Name the blood parasite species.
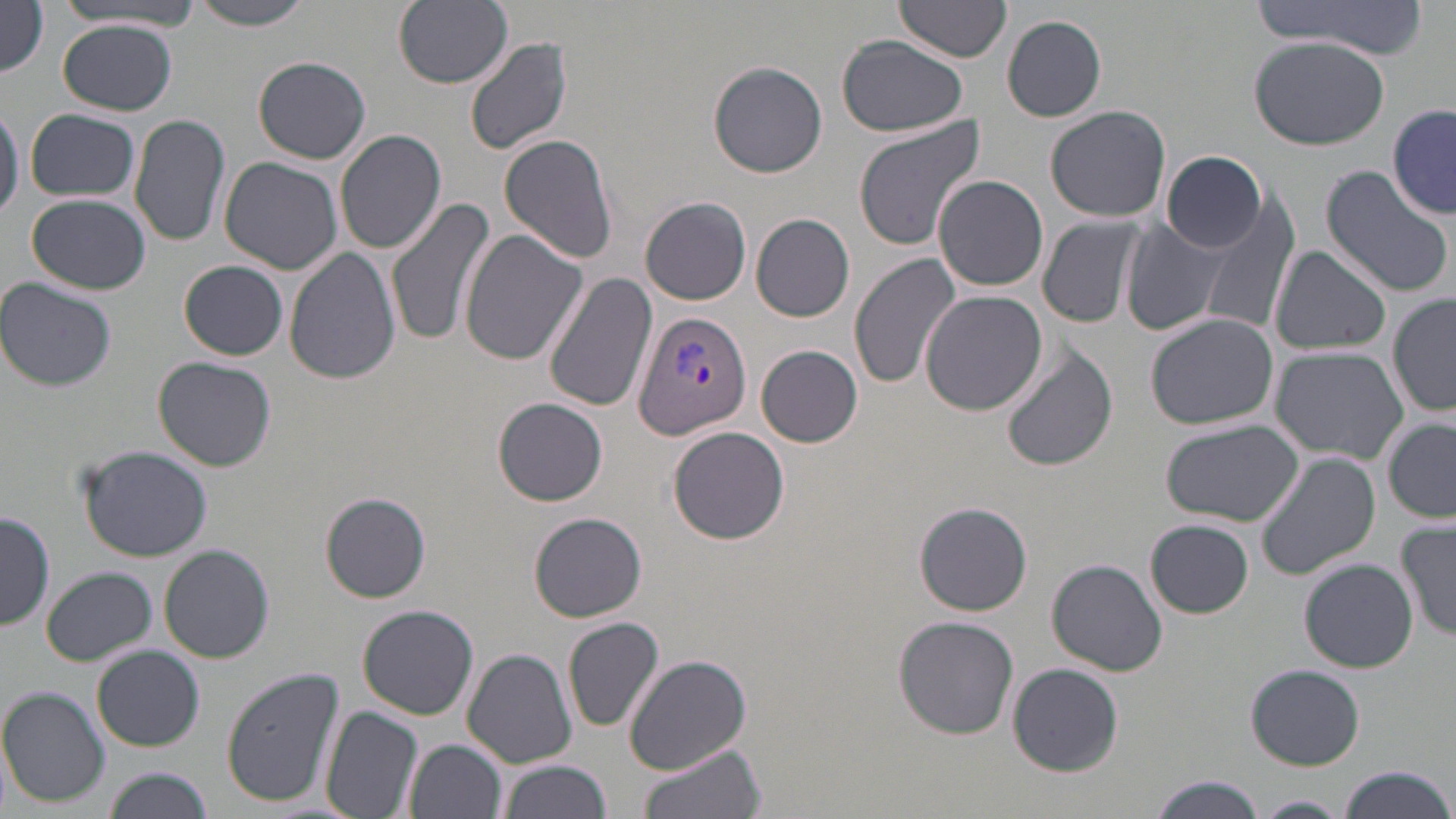

Plasmodium vivax.

Approximate bounding boxes as named x1/y1/x2/y2 corners in pixels. Plasmodium vivax-infected red blood cell locations: (x1=634, y1=312, x2=752, y2=437). Uninfected red blood cell locations: (x1=395, y1=0, x2=513, y2=89), (x1=1253, y1=0, x2=1431, y2=59), (x1=895, y1=1, x2=1013, y2=66), (x1=0, y1=2, x2=50, y2=77), (x1=184, y1=2, x2=319, y2=30), (x1=54, y1=4, x2=201, y2=32), (x1=1002, y1=15, x2=1107, y2=122), (x1=60, y1=20, x2=180, y2=114), (x1=464, y1=33, x2=574, y2=157), (x1=1249, y1=34, x2=1390, y2=150), (x1=837, y1=35, x2=969, y2=137), (x1=253, y1=56, x2=371, y2=164), (x1=707, y1=60, x2=828, y2=177), (x1=0, y1=101, x2=23, y2=225), (x1=1043, y1=104, x2=1170, y2=222), (x1=1389, y1=105, x2=1456, y2=218), (x1=24, y1=109, x2=141, y2=201), (x1=128, y1=111, x2=229, y2=248), (x1=852, y1=115, x2=988, y2=251), (x1=335, y1=128, x2=447, y2=254), (x1=498, y1=134, x2=619, y2=264), (x1=1162, y1=151, x2=1266, y2=252), (x1=220, y1=157, x2=343, y2=276), (x1=1318, y1=165, x2=1455, y2=298), (x1=934, y1=175, x2=1048, y2=291), (x1=27, y1=194, x2=150, y2=295), (x1=1200, y1=195, x2=1301, y2=339), (x1=387, y1=196, x2=497, y2=345), (x1=640, y1=196, x2=752, y2=305), (x1=750, y1=212, x2=857, y2=322), (x1=1038, y1=216, x2=1143, y2=329), (x1=1122, y1=220, x2=1228, y2=336), (x1=458, y1=228, x2=589, y2=366), (x1=1270, y1=245, x2=1391, y2=356), (x1=283, y1=246, x2=401, y2=385), (x1=849, y1=252, x2=961, y2=388), (x1=179, y1=260, x2=288, y2=360), (x1=545, y1=273, x2=659, y2=415), (x1=0, y1=279, x2=118, y2=393), (x1=919, y1=288, x2=1047, y2=416), (x1=1387, y1=294, x2=1455, y2=418), (x1=1144, y1=314, x2=1279, y2=431), (x1=755, y1=345, x2=864, y2=447), (x1=1003, y1=345, x2=1119, y2=472), (x1=1269, y1=346, x2=1410, y2=461), (x1=152, y1=355, x2=277, y2=472), (x1=492, y1=397, x2=609, y2=507), (x1=1159, y1=419, x2=1301, y2=526), (x1=1384, y1=419, x2=1455, y2=522), (x1=667, y1=425, x2=789, y2=545), (x1=77, y1=445, x2=214, y2=563), (x1=1257, y1=449, x2=1383, y2=580), (x1=320, y1=492, x2=433, y2=603), (x1=915, y1=501, x2=1034, y2=615), (x1=1, y1=510, x2=54, y2=632), (x1=528, y1=512, x2=647, y2=622), (x1=1147, y1=519, x2=1254, y2=619), (x1=1396, y1=522, x2=1455, y2=641), (x1=158, y1=544, x2=275, y2=664), (x1=1301, y1=558, x2=1419, y2=671), (x1=1046, y1=559, x2=1168, y2=678), (x1=41, y1=566, x2=157, y2=666), (x1=357, y1=604, x2=479, y2=720), (x1=895, y1=616, x2=1020, y2=739), (x1=563, y1=617, x2=665, y2=733), (x1=92, y1=646, x2=205, y2=752), (x1=463, y1=649, x2=578, y2=767), (x1=623, y1=654, x2=752, y2=772), (x1=1007, y1=663, x2=1126, y2=775), (x1=1246, y1=664, x2=1364, y2=770), (x1=220, y1=667, x2=346, y2=807), (x1=1, y1=687, x2=113, y2=806), (x1=321, y1=705, x2=424, y2=819), (x1=405, y1=737, x2=508, y2=819), (x1=637, y1=745, x2=766, y2=819), (x1=498, y1=760, x2=614, y2=819), (x1=1338, y1=764, x2=1455, y2=819), (x1=104, y1=767, x2=214, y2=819), (x1=1148, y1=775, x2=1266, y2=818), (x1=1250, y1=795, x2=1354, y2=818). May-Grünwald-Giemsa stain. Thin blood smear. One field of a larger specimen. Optical microscopy. Image is 1456×819 pixels. 1000x magnification.